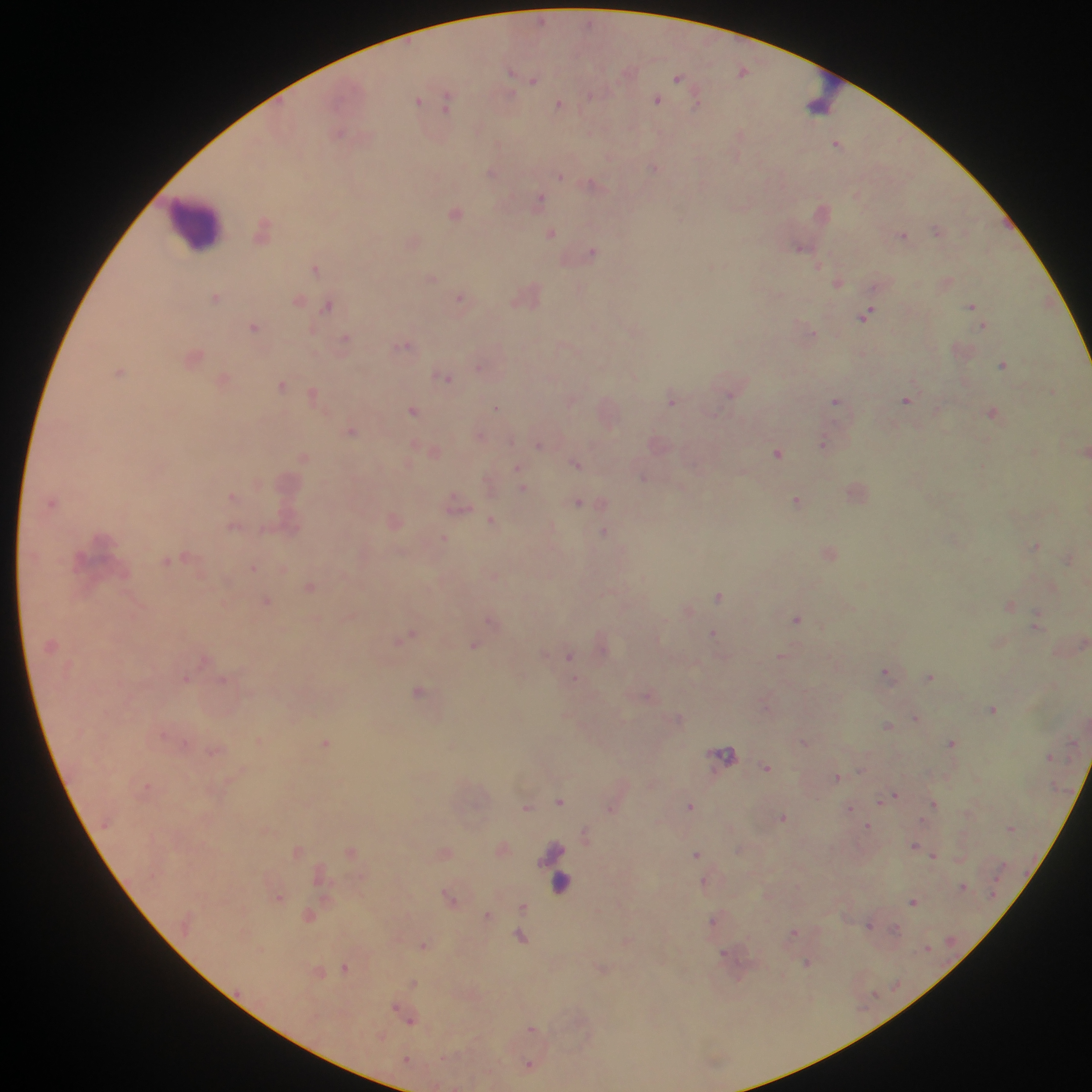 Approximate centers as x y in pixels. Leukocyte locations (subset; some below the resolvable size): 826 96; 197 223; 560 887. Malaria parasite locations: 541 20; 743 71; 511 72; 678 78; 534 80; 590 96; 417 100; 656 100; 448 101; 696 104; 559 105; 339 132; 739 133; 836 144; 654 168; 491 172; 561 176; 593 184; 539 199; 455 213; 681 219; 263 229; 936 230; 552 233; 903 235; 800 246; 593 251; 819 266; 314 267; 431 277; 838 282; 216 297; 460 298; 299 300; 327 305; 971 306; 867 313; 254 326; 983 326; 312 331; 812 333; 345 338; 403 345; 193 357; 1003 365; 478 367; 120 372; 448 378; 223 380; 282 385; 313 394; 731 396; 671 400; 906 400; 835 401; 496 407; 413 410; 992 413; 351 432; 823 443; 538 445; 778 453; 303 457; 576 463; 517 468; 643 477; 522 488; 231 495; 797 501; 578 503; 458 504; 491 520; 233 527; 604 531; 443 538; 1036 546; 169 560; 252 568; 310 587; 718 597; 266 602; 1010 605; 797 619; 490 620; 1035 626; 713 633; 408 635; 474 646; 569 656; 780 656; 886 671; 929 676; 186 679; 419 691; 648 697; 993 709; 915 717; 678 718; 887 725; 259 741; 951 742; 325 743; 804 743; 725 754; 767 768; 838 777; 890 797; 560 801; 934 804; 689 806; 527 808; 850 809; 783 818; 867 825; 1010 828; 585 834; 914 847; 922 851; 695 854; 933 855; 703 881; 963 886; 449 896; 279 897; 913 902; 522 907; 486 915; 713 920; 869 925; 895 929; 794 932; 521 937; 423 946; 725 955; 807 963; 346 967; 414 983; 399 1012; 408 1019; 532 1028; 528 1064. Single field of view. Photographed through a microscope with a mobile-phone camera. Image is 1092×1092 pixels. Collected in Ghana. Thick blood film.